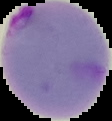 Image is 112×121 pixels. From a thin blood film. Malaria status: parasitized. The area outside the segmented cell region is set to black.